Comment on the morphology of the erythrocytes.
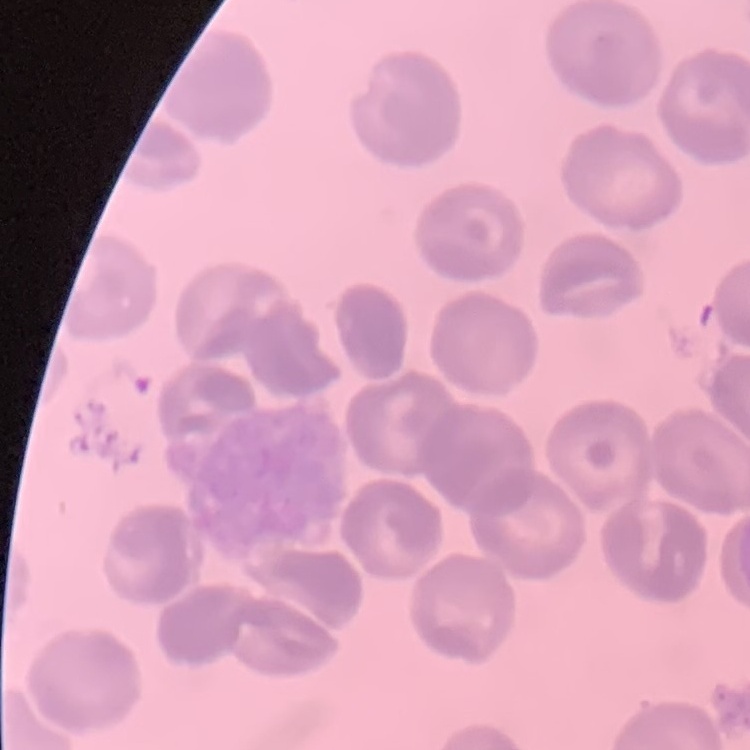

They show no rouleaux formation.

Summary:
  - Image type: square crop of a larger photomicrograph
  - Preparation: thin blood smear
  - Stain: Field's or Giemsa